Outline each uninfected red blood cell.
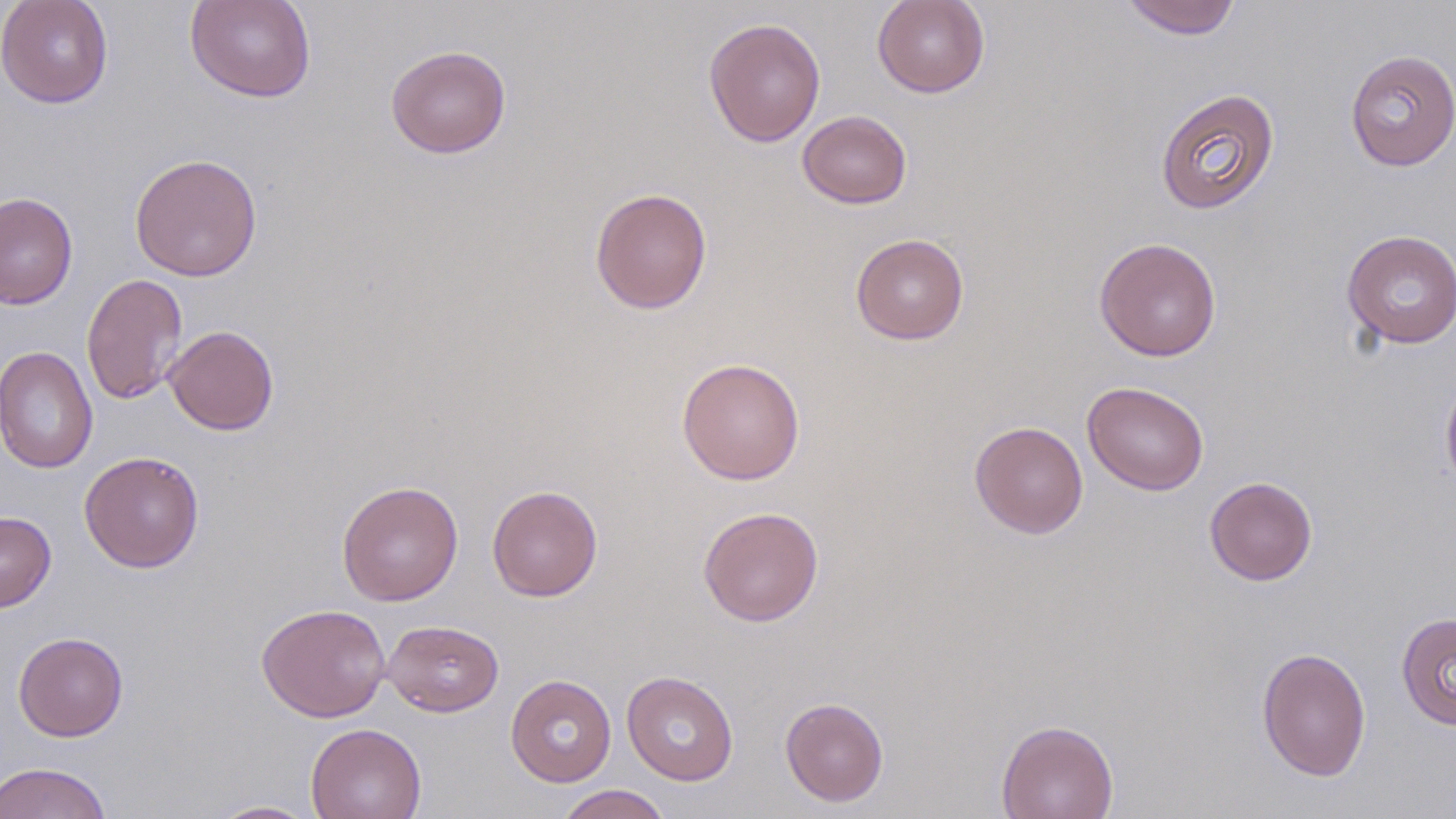

Approximate bounding boxes as (x1, y1, x2, y2) in pixels.
Uninfected red blood cells: (0, 0, 114, 109), (185, 0, 316, 103), (872, 0, 990, 98), (1120, 0, 1242, 39), (703, 17, 826, 147), (385, 44, 512, 159), (1344, 49, 1456, 171), (1155, 88, 1280, 215), (797, 110, 912, 209), (129, 153, 263, 281), (589, 187, 712, 314), (0, 192, 78, 309), (1341, 229, 1456, 349), (850, 233, 969, 345), (1094, 236, 1222, 362), (81, 273, 188, 405), (164, 325, 279, 436), (0, 346, 98, 474), (676, 357, 805, 485), (1440, 370, 1456, 494), (1082, 380, 1209, 496), (969, 420, 1088, 539), (79, 450, 205, 573), (1204, 476, 1318, 586), (337, 480, 463, 606), (487, 484, 603, 601), (697, 506, 824, 626), (0, 511, 56, 612), (256, 603, 391, 723), (1396, 612, 1456, 731), (381, 619, 504, 717), (13, 631, 128, 741), (1256, 646, 1371, 782), (622, 670, 739, 786), (506, 674, 617, 787), (780, 697, 888, 807), (996, 719, 1119, 819), (305, 723, 427, 819), (0, 761, 114, 819), (554, 784, 672, 819), (207, 800, 319, 818).

slide-level diagnosis = no evidence of blood parasites
magnification = 1000x
modality = optical microscopy
field of view = single
preparation = thin blood film
stain = May-Grünwald-Giemsa
image size = 1456×819 pixels